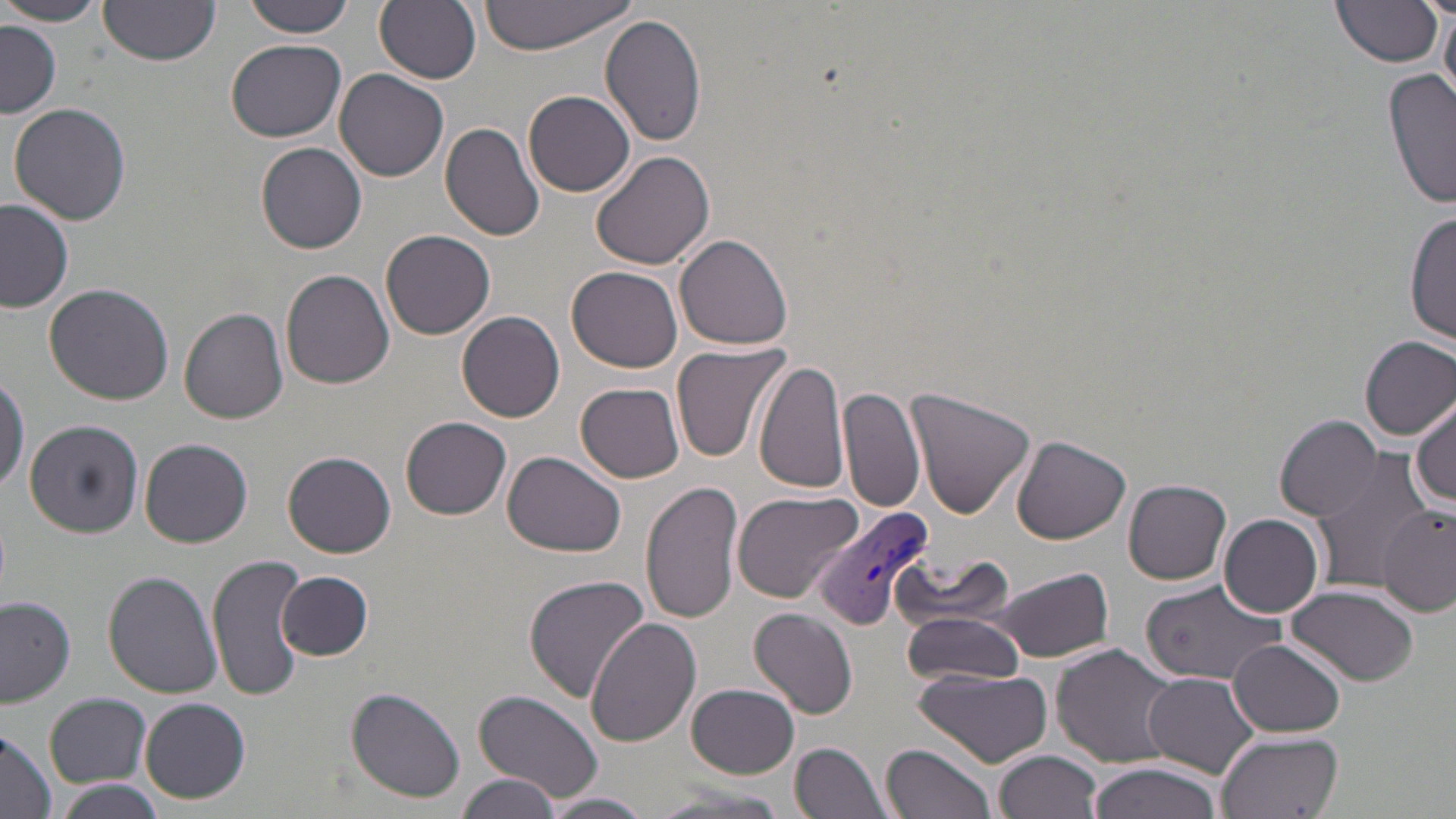
Summary:
  - Coordinate format: approximate bounding boxes as [x1, y1, x2, y2] in pixels
  - Plasmodium vivax-infected red blood cell locations: [811, 507, 937, 630]
  - Uninfected red blood cell locations: [0, 0, 111, 28], [99, 0, 222, 65], [242, 0, 360, 38], [479, 0, 636, 56], [375, 1, 482, 84], [1331, 1, 1447, 68], [1439, 3, 1456, 105], [601, 14, 710, 149], [1, 19, 60, 119], [227, 38, 347, 143], [335, 68, 449, 182], [1384, 71, 1455, 209], [524, 90, 634, 198], [9, 102, 131, 225], [440, 122, 549, 242], [256, 141, 369, 254], [590, 150, 716, 270], [0, 198, 75, 313], [1407, 209, 1456, 347], [381, 229, 496, 340], [674, 232, 794, 350], [568, 266, 683, 373], [280, 268, 395, 389], [44, 283, 174, 406], [179, 308, 290, 425], [456, 311, 566, 422], [1360, 336, 1456, 439], [671, 341, 790, 461], [754, 358, 853, 497], [0, 366, 29, 500], [576, 381, 685, 482], [838, 386, 926, 517], [903, 388, 1037, 519], [1412, 399, 1456, 509], [1275, 415, 1384, 522], [23, 416, 145, 536], [401, 416, 512, 520], [1011, 435, 1129, 543], [139, 437, 253, 548], [283, 450, 397, 557], [503, 450, 626, 558], [1312, 452, 1435, 585], [1123, 478, 1232, 585], [640, 479, 744, 625], [730, 489, 863, 604], [1377, 506, 1455, 615], [1220, 514, 1326, 616], [892, 551, 1016, 633], [208, 552, 307, 701], [989, 566, 1115, 662], [103, 570, 224, 698], [276, 571, 374, 659], [523, 574, 649, 702], [1139, 578, 1286, 685], [1285, 585, 1420, 687], [0, 595, 76, 706], [750, 608, 859, 719], [900, 612, 1026, 685], [586, 619, 701, 749], [1230, 640, 1346, 738], [1051, 644, 1182, 769], [914, 668, 1054, 767], [1144, 672, 1259, 777], [685, 683, 799, 778], [345, 687, 466, 804], [474, 688, 604, 805], [46, 692, 151, 787], [139, 698, 250, 802], [0, 729, 57, 819], [1216, 732, 1346, 819], [790, 741, 895, 819], [882, 741, 998, 819], [993, 750, 1103, 819], [1085, 761, 1224, 819], [455, 773, 562, 819], [48, 779, 168, 818], [650, 784, 789, 819], [545, 793, 650, 819]
  - Slide-level diagnosis: Plasmodium vivax
  - Magnification: 1000x
  - Image size: 1456×819 pixels
  - Field of view: one of a larger specimen
  - Modality: optical microscopy
  - Preparation: thin blood smear
  - Stain: May-Grünwald-Giemsa